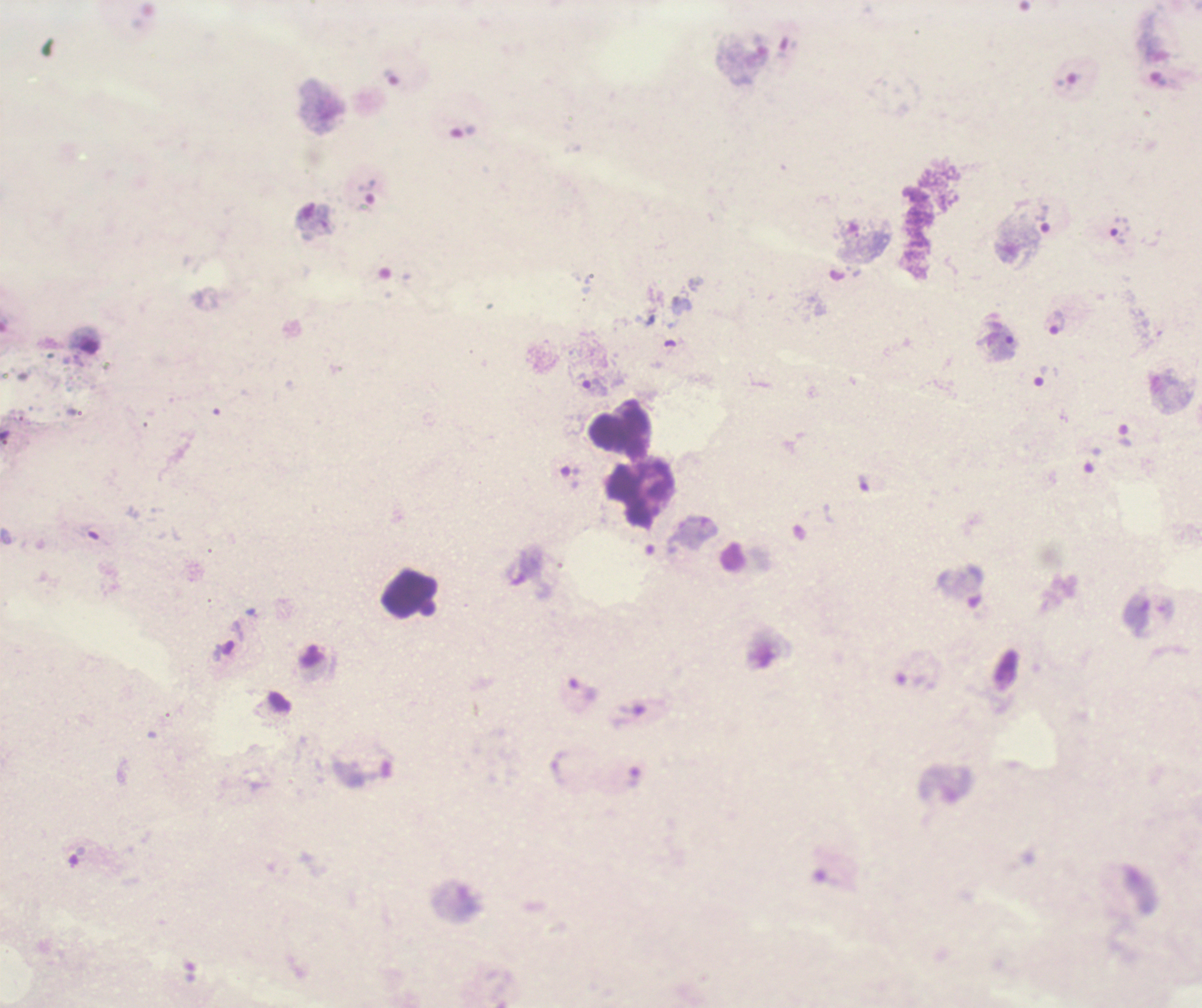
{
  "field_of_view": "one from this slide",
  "magnification": "100x",
  "coloration_quality": "bad",
  "trophozoite_locations": "approximate centers as [x, y] in pixels: [463, 132], [367, 192], [1042, 218], [1057, 322], [1047, 376], [591, 386], [1124, 436], [1093, 460], [570, 476], [630, 717]",
  "background_quality": "poor",
  "leukocyte_locations": "approximate centers as [x, y] in pixels: [619, 434], [631, 498]",
  "image_size": "1202×1008 pixels",
  "result": "Plasmodium parasites identified",
  "preparation": "thick blood film",
  "context": "previously used in a real diagnosis",
  "stain": "Romanowsky"
}